Report the malaria status of this cell.
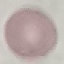
Uninfected.

Thin blood film. Acquired by smartphone through the microscope eyepiece. Cell patch, automatically extracted from a larger field of view and resized to 64 × 64 pixels. Giemsa-stained preparation.